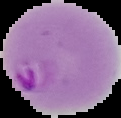
The area outside the segmented cell region is set to black. Image is 121×118 pixels. Malaria status: parasitized. From a thin blood smear.